State the preparation type.
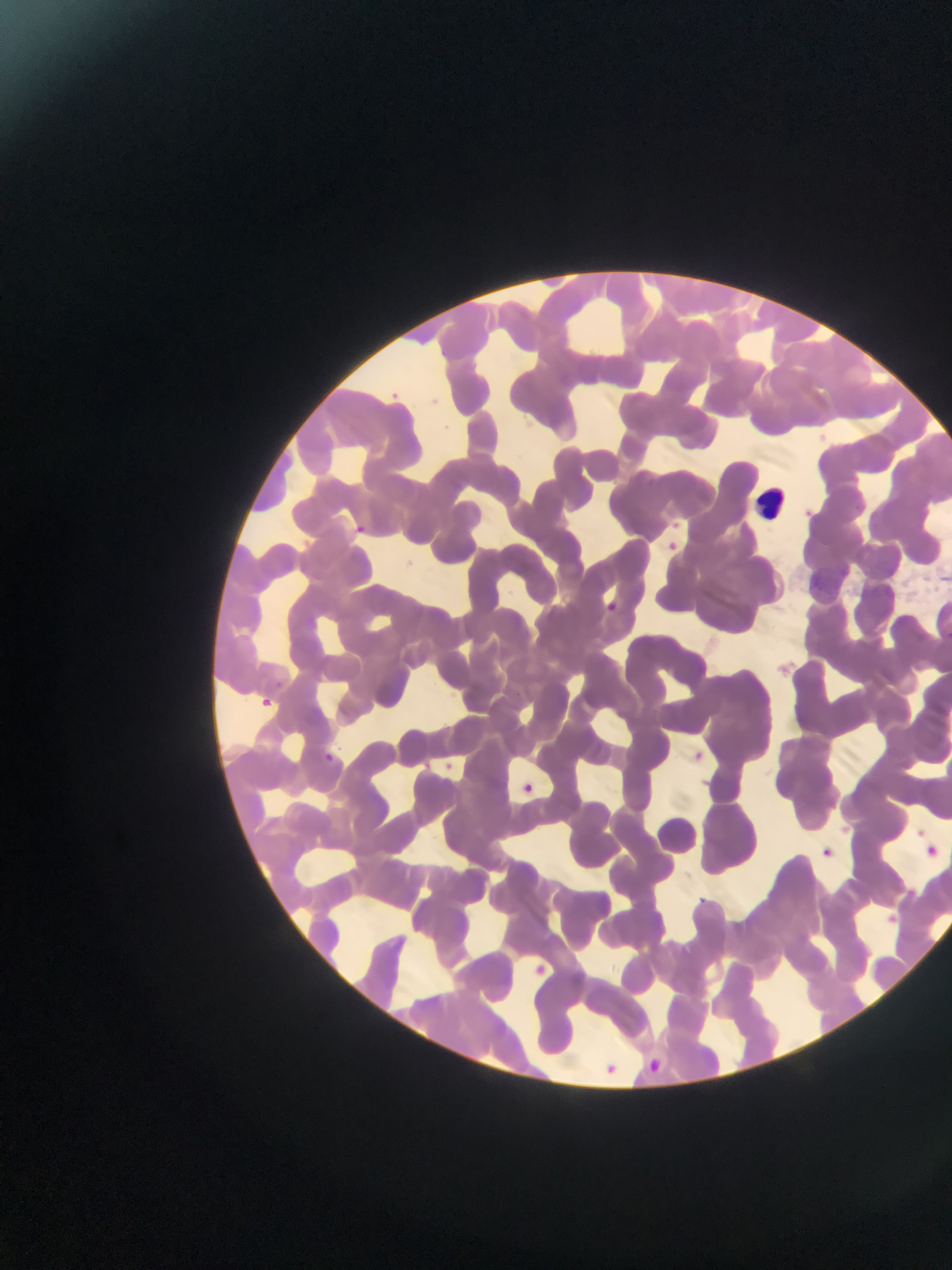

This is a thin smear.

Approximate bounding boxes as (left, top, right, bottom) in pixels. Malaria parasite locations: (391, 387, 401, 399), (819, 433, 829, 444), (802, 504, 815, 524), (668, 519, 683, 541), (353, 521, 372, 545), (664, 539, 691, 560), (603, 597, 640, 637), (270, 672, 306, 696), (256, 694, 274, 712), (687, 741, 713, 761), (312, 743, 345, 771), (440, 748, 463, 774), (517, 780, 540, 799), (919, 836, 938, 861), (816, 840, 845, 867), (906, 881, 920, 898), (694, 892, 716, 911), (887, 908, 903, 927), (529, 961, 547, 977), (600, 1058, 620, 1075), (645, 1058, 668, 1072). Leukocyte locations: (753, 484, 792, 523). Photographed through a microscope with a mobile-phone camera. Image is 952×1270 pixels. One field of view. Sample from Ghana.